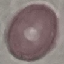
Malaria status: uninfected. Acquired by smartphone through the microscope eyepiece. Thin blood film. Giemsa-stained preparation. Cell patch, automatically extracted from a larger field of view and resized to 64 × 64 pixels.